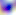
Photomicrograph. Toxoplasma gondii is shown. Captured at 400x magnification.